Locate every Plasmodium parasite.
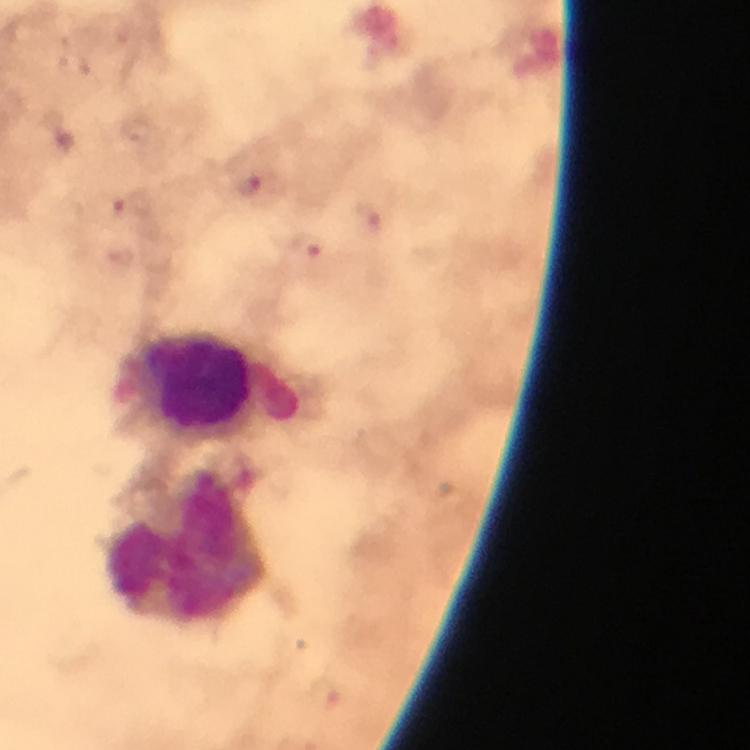
Approximate object centers, in pixels from the top-left corner.
Plasmodium parasites: (x=252, y=184), (x=366, y=221), (x=306, y=244), (x=326, y=693).

Leukocyte locations: (x=194, y=381), (x=187, y=545). Photographed with a smartphone mounted on the microscope. A crop from one field of view. Giemsa-stained preparation. Immersion oil was used. From a diagnostic examination for malaria. Thick smear. At 100x magnification. Image is 750×750 pixels.